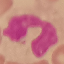
Malaria status: uninfected. Thin smear of blood. Automatically extracted cell patch, resized to 64 × 64 pixels. Giemsa stain. Photographed with a smartphone camera at the microscope eyepiece.